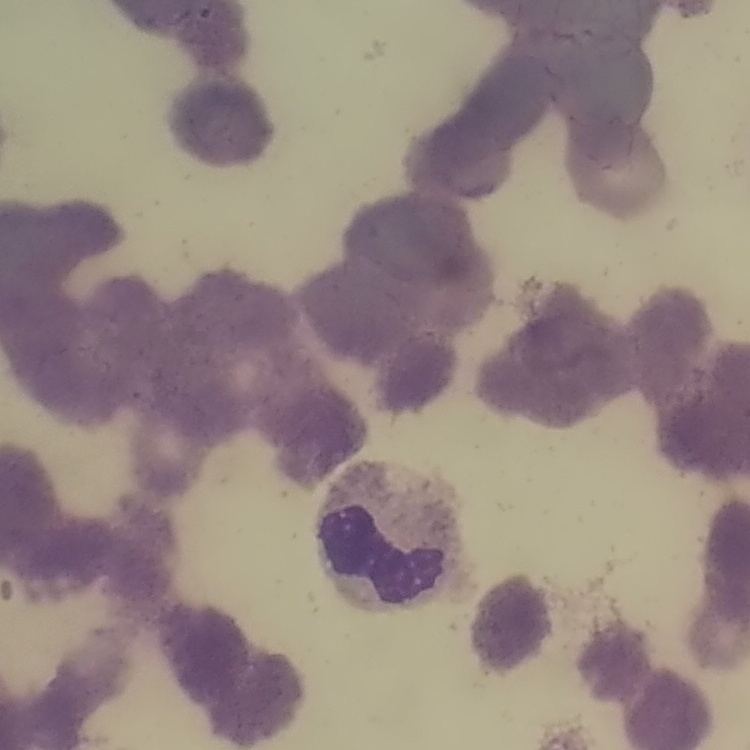

Summary:
  - Erythrocyte morphology: rouleaux formation
  - Stain: Field's or Giemsa
  - Image type: square crop of a larger photomicrograph
  - Preparation: thin blood smear